Report the malaria status of this cell.
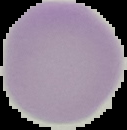
Uninfected.

Summary:
  - Preparation: thin blood smear
  - Image type: cell region segmented out of the field of view; surrounding area masked to black
  - Image size: 127×130 pixels